Report the malaria status of this cell.
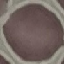
Uninfected.

Acquired by smartphone through the microscope eyepiece. Automatically extracted cell patch, resized to 64 × 64 pixels. Giemsa-stained preparation. Thin blood film.